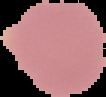

Summary:
  - Image size: 106×97 pixels
  - Result: no Plasmodium parasites seen
  - Preparation: thin blood smear
  - Image type: segmented cell region with the area outside set to black